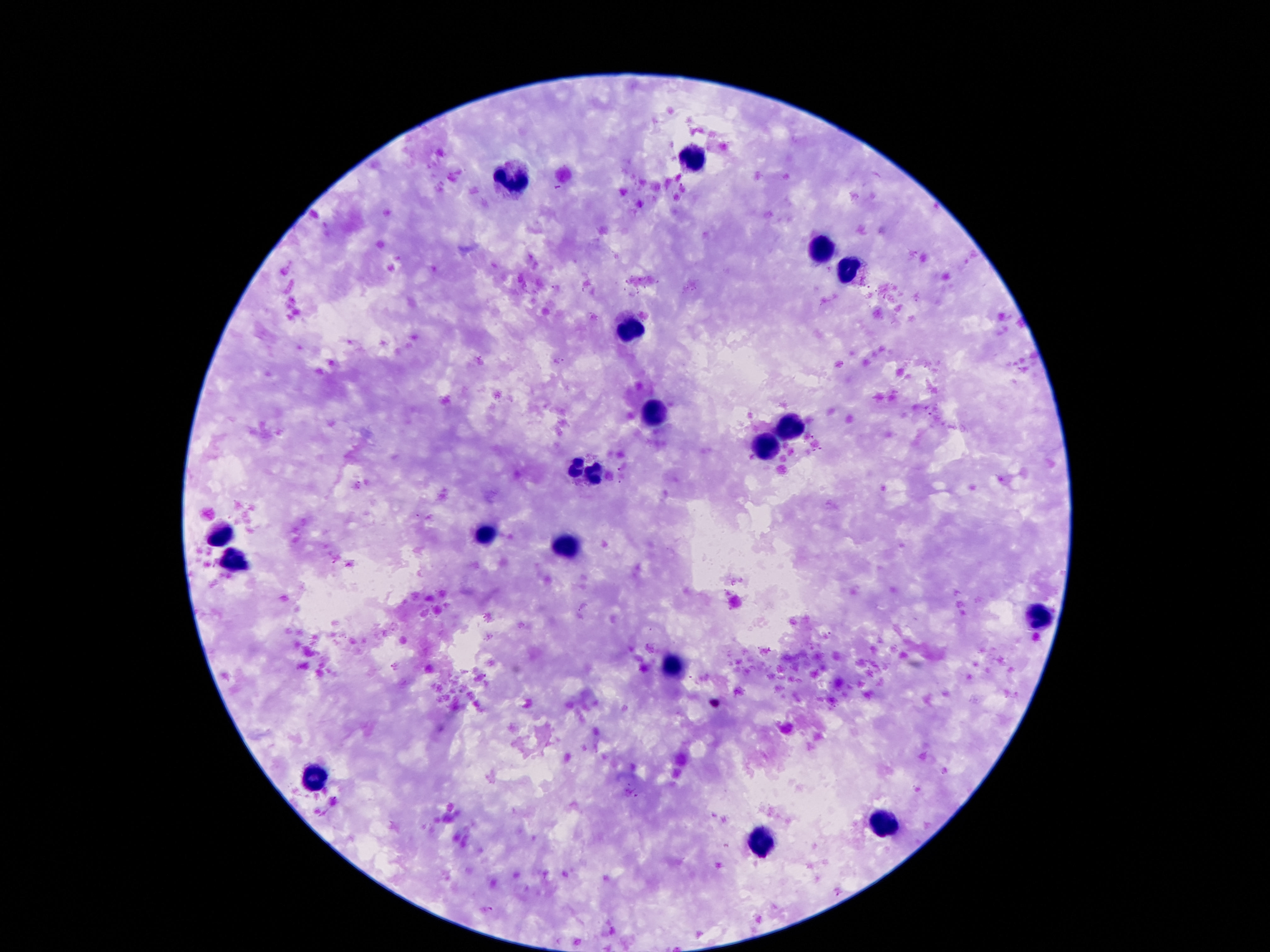

{
  "preparation": "thick blood smear",
  "leukocyte_locations": "approximate centers as {x, y} in pixels: {695, 159}, {516, 179}, {817, 256}, {849, 273}, {628, 329}, {649, 415}, {789, 427}, {768, 450}, {586, 470}, {488, 536}, {222, 539}, {567, 547}, {238, 560}, {1041, 616}, {674, 665}, {313, 778}, {882, 823}, {758, 844}",
  "image_size": "1270×952 pixels",
  "stain": "Giemsa",
  "capture": "smartphone camera through the microscope eyepiece",
  "magnification": "100x",
  "field_of_view": "one from this slide",
  "patient_malaria_status": "not infected"
}